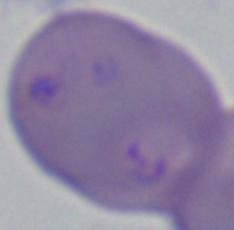

Summary:
  - Modality: photomicrograph
  - Identification: Babesia
  - Magnification: 1000x